Name the cell type shown.
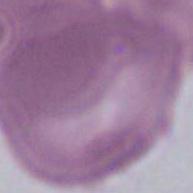
An erythrocyte.

magnification = 1000x
modality = photomicrograph